Locate and identify every blood parasite.
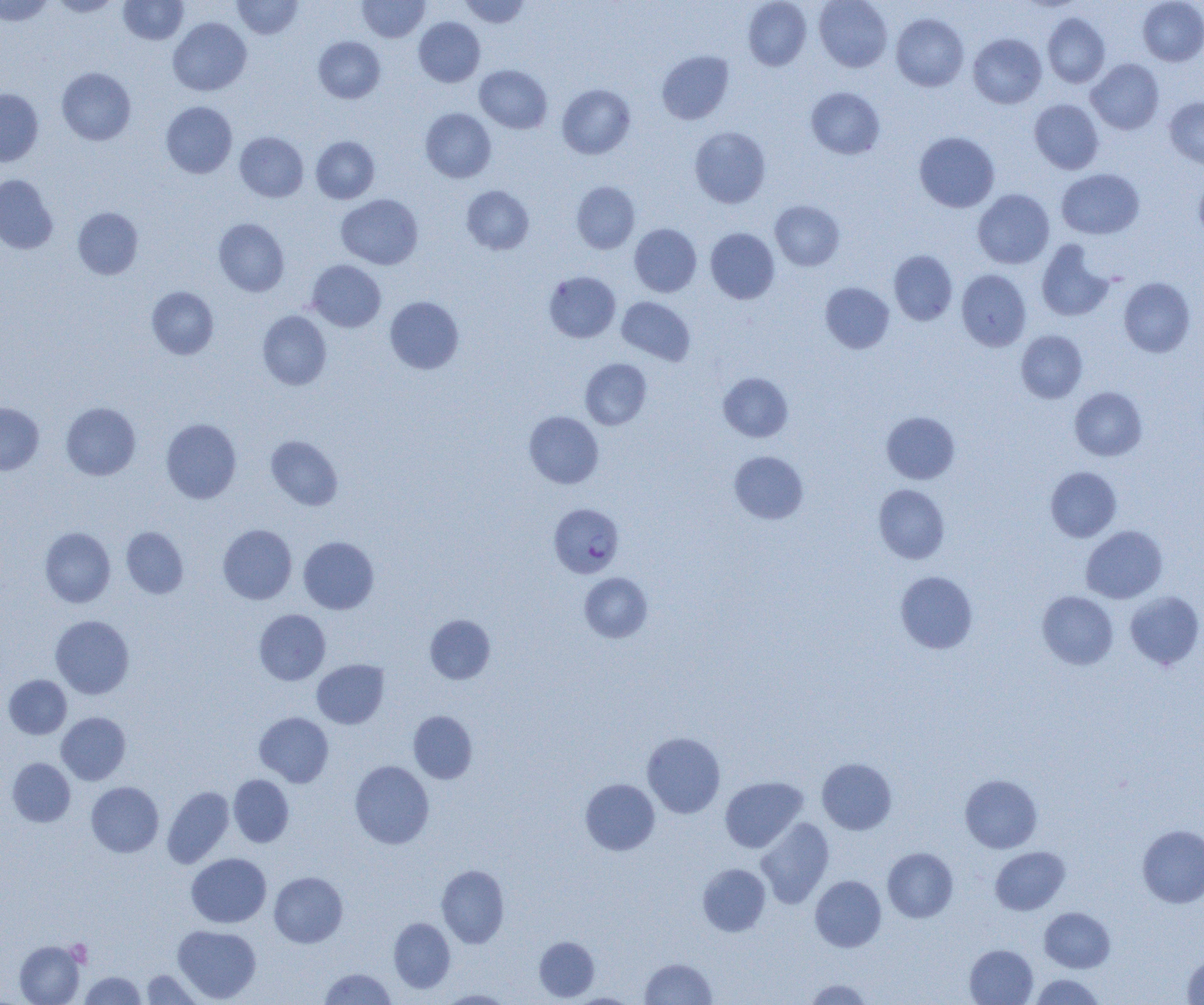

Approximate bounding boxes as (x1, y1, x2, y2) in pixels.
Plasmodium falciparum-infected red blood cells: (549, 503, 624, 578).
No Plasmodium ovale, Plasmodium malariae, Plasmodium vivax, Babesia divergens, or Trypanosoma brucei observed.

Summary:
  - Uninfected red blood cell locations: (0, 0, 53, 25), (51, 0, 120, 17), (118, 0, 188, 44), (232, 0, 302, 39), (357, 0, 430, 42), (460, 0, 530, 28), (743, 0, 811, 70), (814, 0, 892, 72), (1138, 0, 1204, 66), (891, 13, 968, 91), (1042, 13, 1110, 87), (169, 17, 251, 95), (414, 17, 485, 87), (968, 33, 1046, 108), (314, 36, 385, 103), (657, 50, 734, 124), (1086, 58, 1164, 134), (475, 65, 552, 133), (57, 67, 136, 145), (557, 84, 635, 159), (806, 87, 884, 159), (0, 89, 43, 166), (1164, 97, 1204, 168), (1030, 99, 1103, 174), (161, 102, 237, 178), (420, 108, 496, 182), (690, 126, 771, 207), (235, 132, 308, 202), (914, 132, 999, 212), (311, 136, 379, 203), (1057, 168, 1144, 239), (1194, 174, 1204, 241), (0, 175, 57, 253), (572, 181, 640, 253), (462, 186, 534, 254), (973, 189, 1054, 269), (336, 194, 423, 269), (770, 200, 844, 270), (73, 207, 143, 279), (214, 218, 289, 296), (630, 224, 701, 296), (705, 228, 779, 303), (1036, 240, 1114, 322), (889, 250, 957, 324), (307, 260, 386, 332), (956, 269, 1030, 351), (544, 271, 620, 342), (1119, 277, 1195, 357), (820, 282, 894, 353), (147, 286, 219, 359), (385, 296, 464, 374), (617, 297, 695, 365), (258, 311, 331, 390), (1016, 330, 1087, 403), (581, 358, 652, 429), (718, 372, 793, 442), (1070, 387, 1147, 461), (61, 402, 140, 480), (0, 403, 44, 475), (524, 411, 604, 488), (881, 411, 960, 483), (161, 418, 241, 503), (266, 435, 342, 510), (730, 451, 808, 523), (1045, 466, 1121, 542), (873, 484, 950, 563), (218, 525, 297, 604), (1081, 525, 1167, 603), (40, 527, 115, 607), (121, 527, 188, 598), (298, 536, 379, 614), (895, 571, 977, 654), (580, 573, 652, 642), (1037, 590, 1118, 669), (1124, 590, 1204, 670), (254, 609, 330, 685), (425, 614, 495, 684), (51, 615, 134, 699), (312, 659, 388, 729), (3, 675, 71, 738), (408, 711, 477, 783), (57, 712, 130, 784), (255, 712, 333, 787), (642, 732, 725, 818), (8, 758, 75, 826), (817, 758, 896, 834), (350, 761, 434, 849), (229, 774, 294, 847), (960, 774, 1042, 853), (720, 776, 807, 853), (581, 779, 660, 855), (86, 782, 163, 857), (162, 786, 234, 868), (756, 818, 834, 908), (1137, 825, 1204, 908), (883, 847, 958, 922), (990, 847, 1070, 915), (186, 853, 271, 928), (698, 863, 770, 936), (437, 865, 509, 947), (269, 872, 348, 947), (810, 876, 886, 952), (1040, 907, 1115, 972), (389, 917, 455, 993), (173, 925, 261, 1003), (534, 936, 599, 1001), (14, 940, 84, 1005), (965, 944, 1038, 1004), (1182, 954, 1204, 1003), (640, 958, 716, 1004), (319, 968, 396, 1005), (141, 969, 203, 1004), (80, 971, 146, 1004), (1030, 974, 1105, 1004), (804, 978, 872, 1005), (438, 990, 514, 1004), (569, 993, 638, 1005)
  - Platelet locations: (67, 939, 92, 967)
  - Slide-level diagnosis: Plasmodium falciparum
  - Preparation: thin blood film
  - Magnification: 1000x
  - Image size: 1204×1005 pixels
  - Modality: light microscopy
  - Field of view: one of a larger specimen